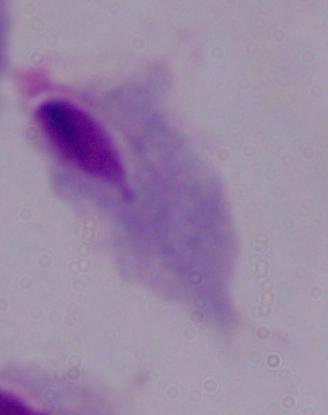

modality = photomicrograph
identification = trichomonad
magnification = 1000x